State the blood parasite species.
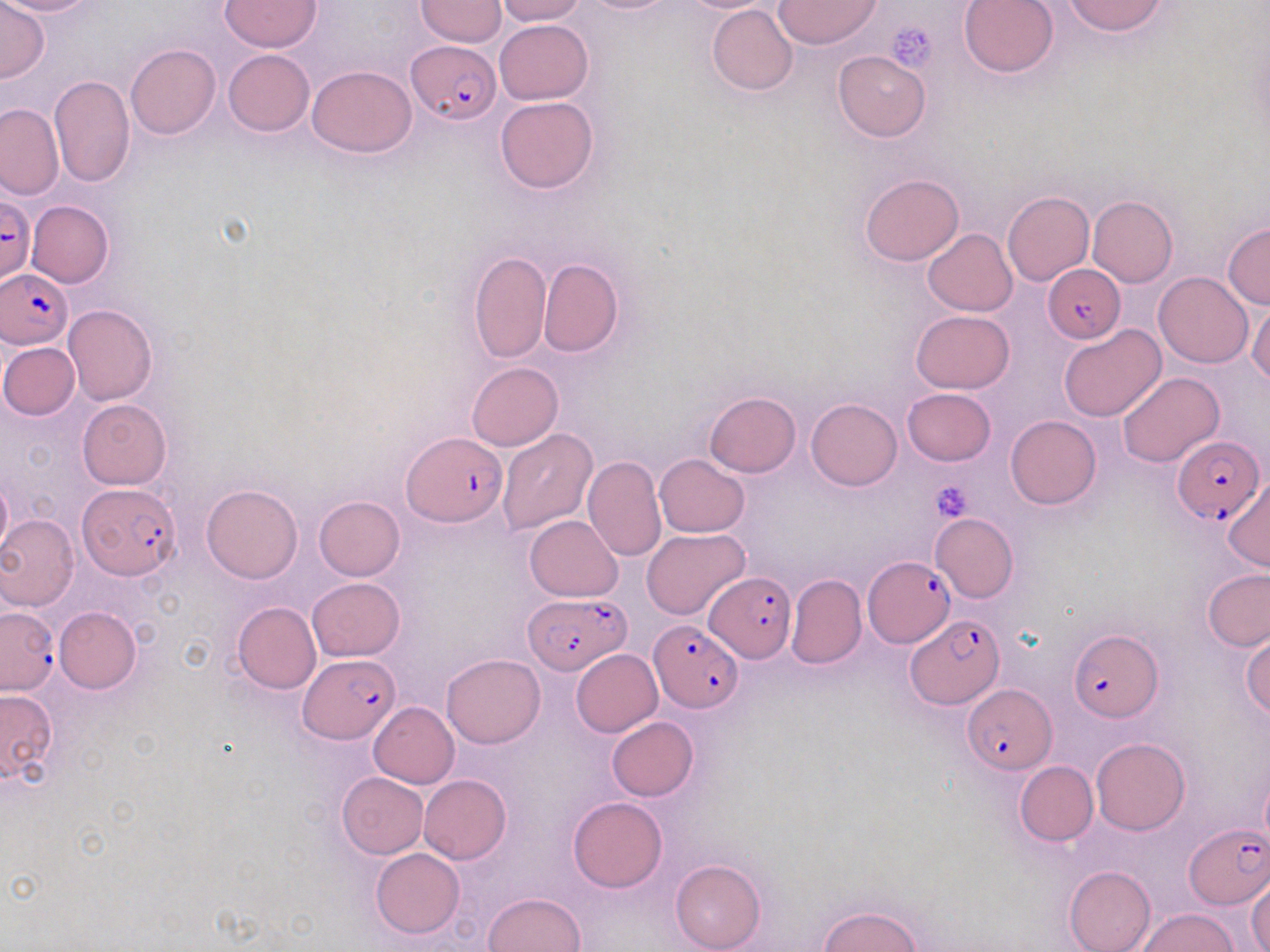

Plasmodium falciparum.

Approximate bounding boxes as (x1, y1, x2, y2) in pixels. Plasmodium falciparum-infected red blood cell locations: (407, 40, 499, 124), (0, 198, 34, 284), (1043, 263, 1126, 343), (1, 269, 73, 345), (401, 432, 506, 528), (1174, 434, 1263, 524), (78, 484, 181, 579), (864, 558, 955, 646), (705, 572, 796, 662), (530, 594, 631, 673), (0, 605, 57, 693), (906, 617, 1005, 707), (648, 620, 744, 713), (1069, 628, 1161, 722), (299, 656, 398, 743), (965, 686, 1057, 773), (1185, 823, 1270, 908). Platelet locations: (885, 19, 939, 72), (929, 480, 975, 525). Uninfected red blood cell locations: (0, 0, 99, 17), (0, 0, 49, 82), (221, 0, 321, 53), (416, 0, 506, 46), (496, 0, 586, 24), (675, 0, 778, 13), (775, 0, 882, 49), (959, 0, 1061, 77), (1063, 0, 1169, 36), (707, 4, 797, 95), (496, 19, 593, 103), (125, 44, 221, 139), (223, 50, 314, 136), (834, 51, 930, 142), (307, 65, 417, 157), (48, 73, 134, 188), (495, 95, 599, 194), (0, 103, 63, 199), (860, 173, 963, 265), (1003, 191, 1094, 285), (1087, 195, 1177, 288), (25, 200, 114, 288), (1223, 222, 1270, 310), (923, 229, 1017, 315), (469, 250, 551, 364), (539, 258, 623, 357), (1154, 271, 1253, 368), (1248, 301, 1270, 386), (63, 304, 157, 405), (910, 310, 1015, 394), (1059, 325, 1166, 422), (0, 342, 79, 420), (467, 362, 563, 451), (1116, 371, 1223, 467), (902, 388, 997, 465), (705, 391, 801, 477), (77, 398, 171, 487), (806, 398, 902, 489), (1006, 415, 1100, 509), (497, 428, 598, 537), (655, 455, 749, 537), (583, 456, 667, 563), (0, 477, 13, 559), (1222, 477, 1269, 571), (200, 486, 302, 584), (314, 496, 405, 580), (930, 513, 1017, 602), (0, 514, 79, 610), (525, 516, 622, 601), (641, 527, 750, 620), (1202, 567, 1270, 652), (786, 574, 866, 669), (306, 578, 405, 661), (232, 601, 320, 694), (54, 606, 141, 692), (1241, 628, 1270, 720), (570, 649, 663, 737), (441, 654, 545, 747), (0, 690, 58, 784), (368, 702, 459, 787), (606, 716, 698, 801), (1090, 739, 1189, 835), (1014, 760, 1098, 846), (337, 773, 428, 858), (419, 775, 511, 863), (568, 797, 666, 893), (370, 848, 464, 939), (670, 858, 765, 952), (1064, 865, 1156, 952), (1248, 875, 1270, 951), (483, 892, 585, 952), (820, 904, 920, 952), (1136, 908, 1239, 951). 1000x magnification. Light microscopy. Thin blood film. Image is 1270×952 pixels. Single field of view. May-Grünwald-Giemsa-stained preparation.